Report the malaria status of this cell.
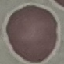

It is uninfected.

stain = Giemsa
image type = automatically extracted cell patch, resized to 64 × 64 pixels
preparation = thin smear
capture = smartphone camera at the microscope eyepiece